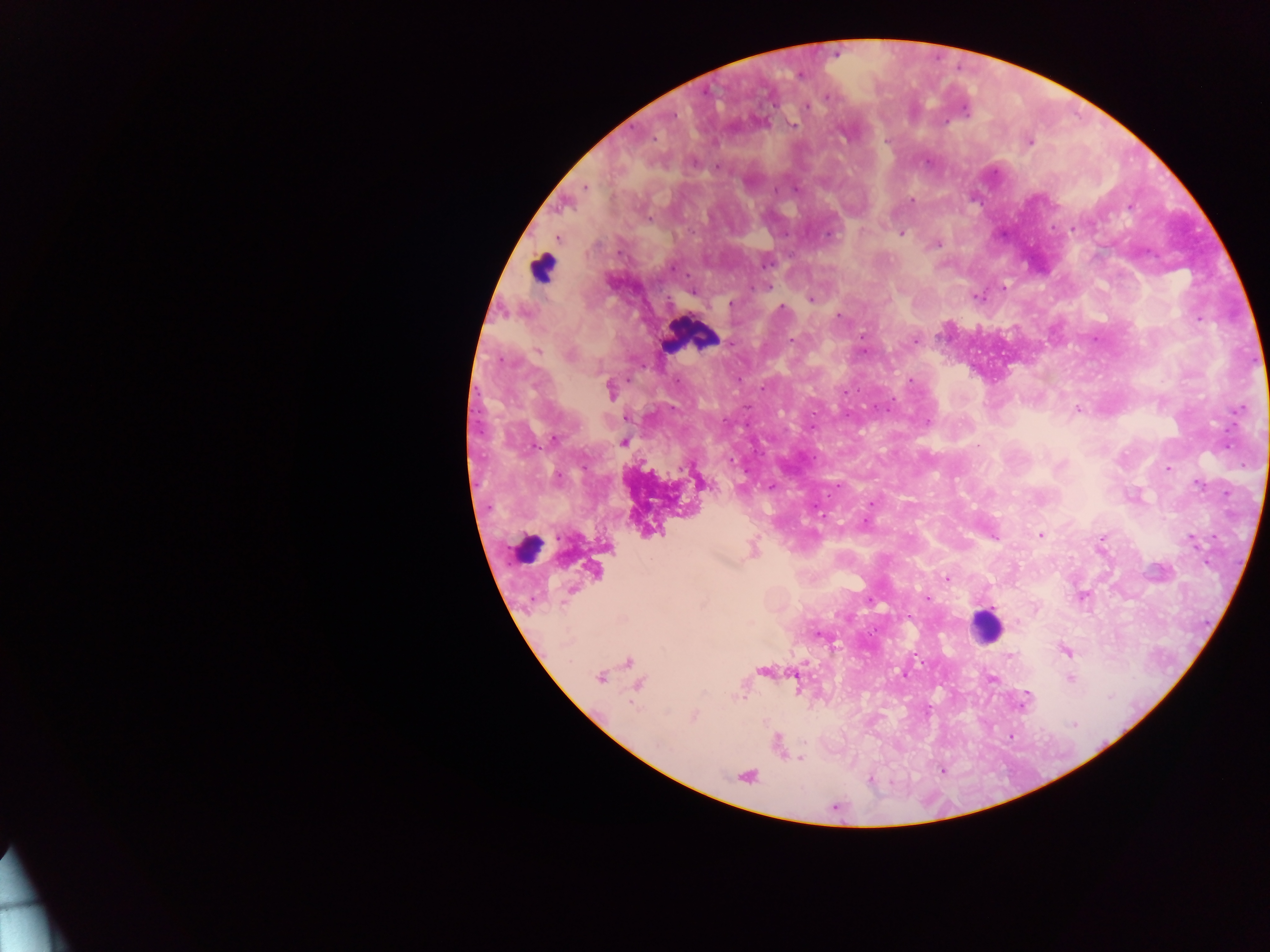
Approximate centers as (x, y) in pixels.
Summary:
  - Leukocyte locations: (542, 268), (691, 335), (986, 626)
  - Plasmodium parasite locations: (800, 75), (827, 96), (807, 107), (965, 111), (672, 116), (794, 125), (885, 140), (1029, 142), (927, 162), (695, 163), (718, 167), (585, 187), (796, 189), (775, 190), (911, 200), (650, 219), (1071, 229), (902, 234), (827, 235), (558, 238), (937, 245), (766, 265), (673, 268), (754, 287), (766, 287), (1003, 287), (692, 292), (977, 296), (810, 299), (730, 303), (782, 307), (839, 316), (1199, 320), (862, 336), (791, 339), (914, 341), (538, 351), (864, 351), (569, 355), (911, 380), (761, 388), (611, 389), (844, 392), (886, 409), (1077, 410), (1239, 410), (626, 419), (928, 422), (812, 427), (555, 438), (623, 442), (979, 445), (731, 462), (1061, 465), (1168, 469), (558, 477), (1198, 485), (771, 486), (871, 504), (1040, 535), (995, 538), (1191, 541), (946, 578), (1082, 596), (927, 599), (870, 601), (1035, 607), (819, 635), (1066, 652), (1010, 656), (905, 675), (600, 678), (992, 679), (1070, 679), (1027, 694), (693, 716), (1073, 723), (800, 759), (870, 780)
  - Object labeled both Plasmodium parasite and leukocyte by the source: (526, 547)
  - Image size: 1270×952 pixels
  - Preparation: thick blood film
  - Field of view: single
  - Country: Ghana
  - Capture: mobile-phone photograph through a microscope